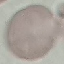
Summary:
  - Result: no malaria parasites seen
  - Capture: smartphone through the microscope eyepiece
  - Stain: Giemsa
  - Preparation: thin blood film
  - Image type: cell patch, automatically extracted from a larger field of view and resized to 64 × 64 pixels